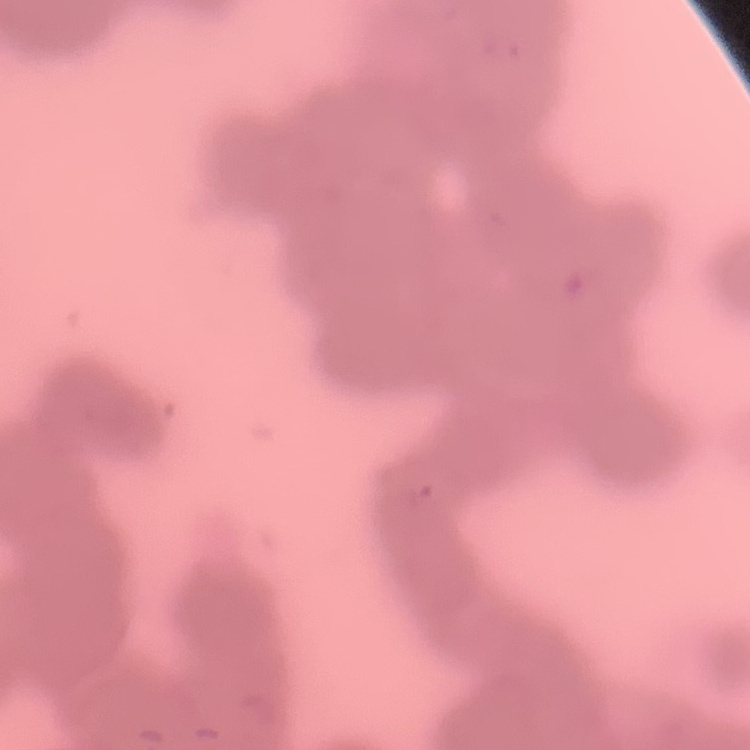

The red blood cells exhibit rouleaux formation. Thin peripheral smear. Square crop of a larger photomicrograph. Stained with either Field's or Giemsa.